Report the malaria status of this cell.
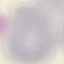
Uninfected.

Summary:
  - Preparation: thin blood smear
  - Image type: cell patch, automatically extracted from a larger field of view and resized to 64 × 64 pixels
  - Capture: smartphone camera at the microscope eyepiece
  - Stain: Giemsa